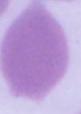

Micrograph. Captured at 1000x magnification. A red blood cell is seen.